Classify this cell by malaria status.
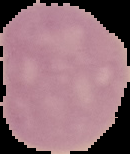

It is uninfected.

Segmented cell region on a black background. Image is 130×154 pixels. From a thin blood film.